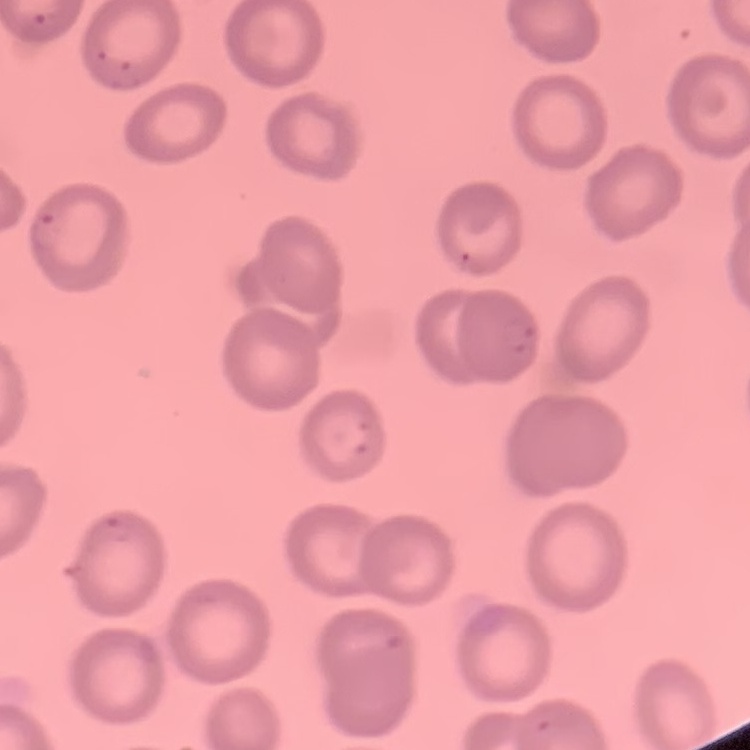
Summary:
  - Red blood cell morphology: no rouleaux formation
  - Stain: Field's or Giemsa
  - Image type: square crop of a larger photomicrograph
  - Preparation: thin peripheral smear